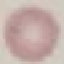
Summary:
  - Malaria status: uninfected
  - Image type: automatically extracted cell patch, resized to 64 × 64 pixels
  - Stain: Giemsa
  - Capture: smartphone through the microscope eyepiece
  - Preparation: thin blood film